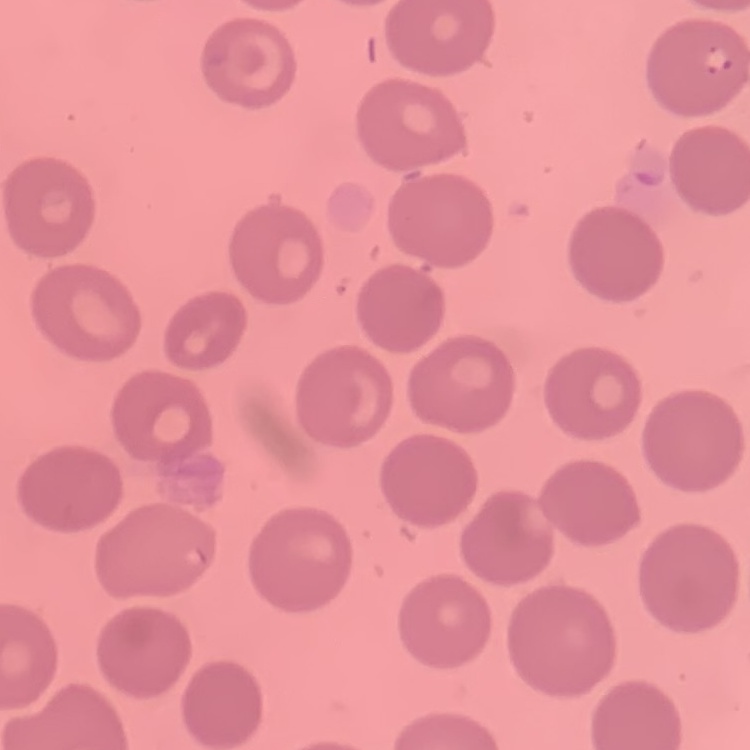
Summary:
  - Erythrocyte morphology: no rouleaux formation
  - Stain: Field's or Giemsa
  - Image type: square crop of a larger photomicrograph
  - Preparation: thin blood film